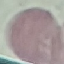

result = no malaria parasites detected
preparation = thin blood film
image type = cell patch, automatically extracted from a larger field of view and resized to 64 × 64 pixels
capture = smartphone through the microscope eyepiece
stain = Giemsa